Point out every malaria parasite and every leukocyte.
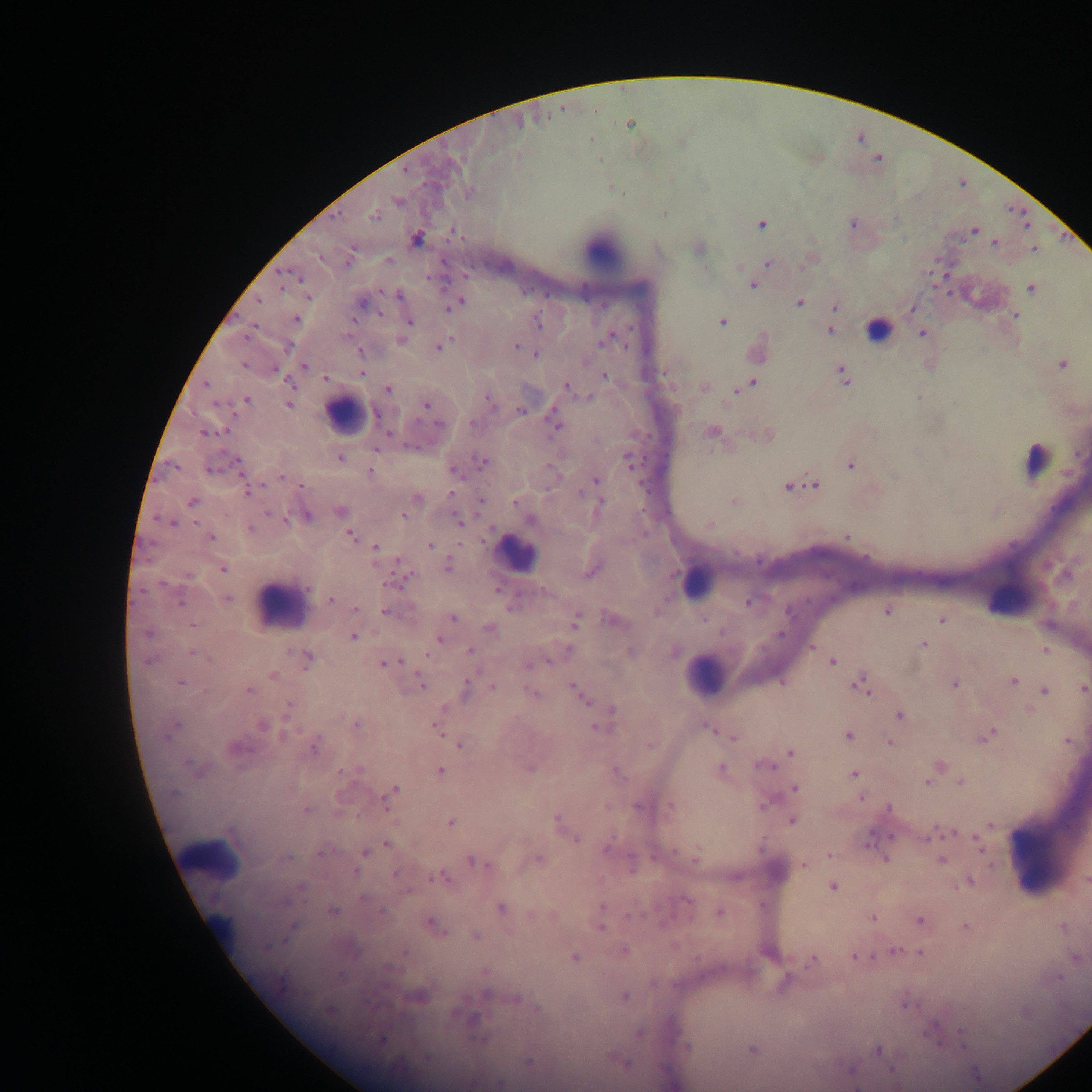
Approximate centers as {x, y} in pixels.
Malaria parasites: {629, 124}, {591, 139}, {405, 170}, {613, 189}, {469, 193}, {397, 201}, {664, 214}, {337, 215}, {375, 217}, {853, 223}, {761, 224}, {973, 230}, {455, 232}, {417, 238}, {995, 243}, {1033, 250}, {320, 257}, {389, 260}, {349, 261}, {768, 263}, {282, 272}, {300, 278}, {753, 286}, {282, 288}, {1031, 289}, {399, 295}, {309, 297}, {258, 301}, {458, 303}, {799, 303}, {361, 304}, {835, 307}, {1016, 315}, {296, 318}, {410, 322}, {722, 322}, {538, 323}, {252, 329}, {830, 331}, {922, 334}, {608, 340}, {401, 341}, {288, 347}, {439, 347}, {516, 347}, {361, 352}, {537, 353}, {1062, 364}, {244, 366}, {305, 367}, {276, 371}, {361, 374}, {844, 376}, {605, 377}, {326, 378}, {752, 383}, {206, 384}, {566, 387}, {703, 388}, {387, 389}, {738, 390}, {588, 397}, {246, 400}, {490, 400}, {217, 404}, {289, 404}, {426, 405}, {520, 411}, {376, 415}, {472, 422}, {439, 425}, {555, 426}, {204, 432}, {712, 433}, {388, 434}, {377, 449}, {340, 458}, {629, 460}, {237, 461}, {482, 462}, {851, 465}, {210, 469}, {455, 471}, {370, 472}, {281, 477}, {596, 479}, {302, 485}, {814, 485}, {787, 487}, {248, 491}, {581, 493}, {452, 495}, {416, 498}, {482, 500}, {601, 501}, {734, 501}, {192, 502}, {514, 503}, {340, 511}, {269, 513}, {307, 516}, {403, 516}, {531, 519}, {458, 520}, {172, 523}, {709, 525}, {250, 529}, {351, 535}, {211, 537}, {847, 537}, {430, 545}, {375, 546}, {447, 566}, {222, 569}, {593, 571}, {188, 575}, {406, 578}, {395, 583}, {306, 588}, {497, 590}, {228, 599}, {330, 599}, {747, 602}, {180, 603}, {356, 608}, {511, 608}, {387, 612}, {887, 612}, {453, 618}, {611, 620}, {942, 620}, {576, 622}, {193, 625}, {489, 629}, {148, 634}, {780, 635}, {354, 637}, {439, 639}, {924, 644}, {812, 648}, {1045, 649}, {470, 650}, {631, 651}, {192, 654}, {427, 655}, {196, 656}, {207, 658}, {308, 659}, {547, 661}, {147, 662}, {832, 662}, {390, 663}, {530, 665}, {273, 675}, {1013, 681}, {181, 682}, {782, 682}, {955, 684}, {422, 685}, {859, 685}, {493, 688}, {1083, 688}, {249, 690}, {467, 690}, {1044, 691}, {532, 693}, {580, 694}, {289, 705}, {442, 709}, {613, 710}, {900, 716}, {356, 724}, {262, 725}, {175, 726}, {599, 727}, {437, 728}, {710, 729}, {286, 734}, {990, 734}, {168, 735}, {849, 736}, {734, 737}, {1068, 742}, {890, 743}, {460, 745}, {650, 745}, {237, 747}, {314, 747}, {791, 753}, {190, 765}, {763, 765}, {529, 768}, {721, 768}, {356, 769}, {440, 770}, {342, 771}, {618, 773}, {853, 774}, {927, 782}, {960, 782}, {795, 788}, {174, 793}, {392, 793}, {388, 798}, {861, 798}, {764, 805}, {637, 806}, {671, 806}, {889, 808}, {306, 810}, {556, 819}, {792, 821}, {451, 823}, {990, 826}, {950, 832}, {930, 836}, {576, 839}, {869, 839}, {979, 843}, {386, 844}, {607, 847}, {675, 851}, {364, 852}, {322, 853}, {830, 854}, {697, 857}, {286, 858}, {538, 859}, {885, 859}, {472, 861}, {941, 861}, {804, 865}, {632, 867}, {356, 872}, {395, 874}, {442, 877}, {1086, 880}, {970, 881}, {302, 886}, {833, 888}, {408, 892}, {363, 898}, {687, 900}, {284, 902}, {602, 907}, {501, 908}, {333, 911}, {381, 911}, {720, 913}, {632, 915}, {530, 917}, {872, 917}, {920, 921}, {433, 926}, {965, 927}, {1062, 928}, {601, 929}, {476, 935}, {266, 947}, {625, 951}, {894, 951}, {405, 953}, {921, 954}, {853, 957}, {1076, 957}, {575, 958}, {812, 960}, {390, 968}, {1059, 977}, {785, 980}, {653, 983}, {487, 994}, {625, 996}, {515, 998}, {906, 1005}, {537, 1008}, {329, 1010}, {474, 1019}, {933, 1032}, {639, 1033}, {962, 1034}, {382, 1040}, {935, 1040}, {686, 1045}, {964, 1046}, {752, 1050}, {878, 1050}, {426, 1057}, {528, 1062}, {624, 1063}, {850, 1070}, {500, 1084}.
Leukocytes: {603, 251}, {879, 328}, {344, 415}, {1037, 460}, {517, 553}, {696, 581}, {1009, 597}, {280, 604}, {705, 674}, {207, 856}, {1047, 859}, {219, 928}.

preparation: thick blood film
capture: mobile-phone photograph through a microscope
field_of_view: single
image_size: 1092×1092 pixels
country: Ghana